Locate every Plasmodium ovale-infected red blood cell.
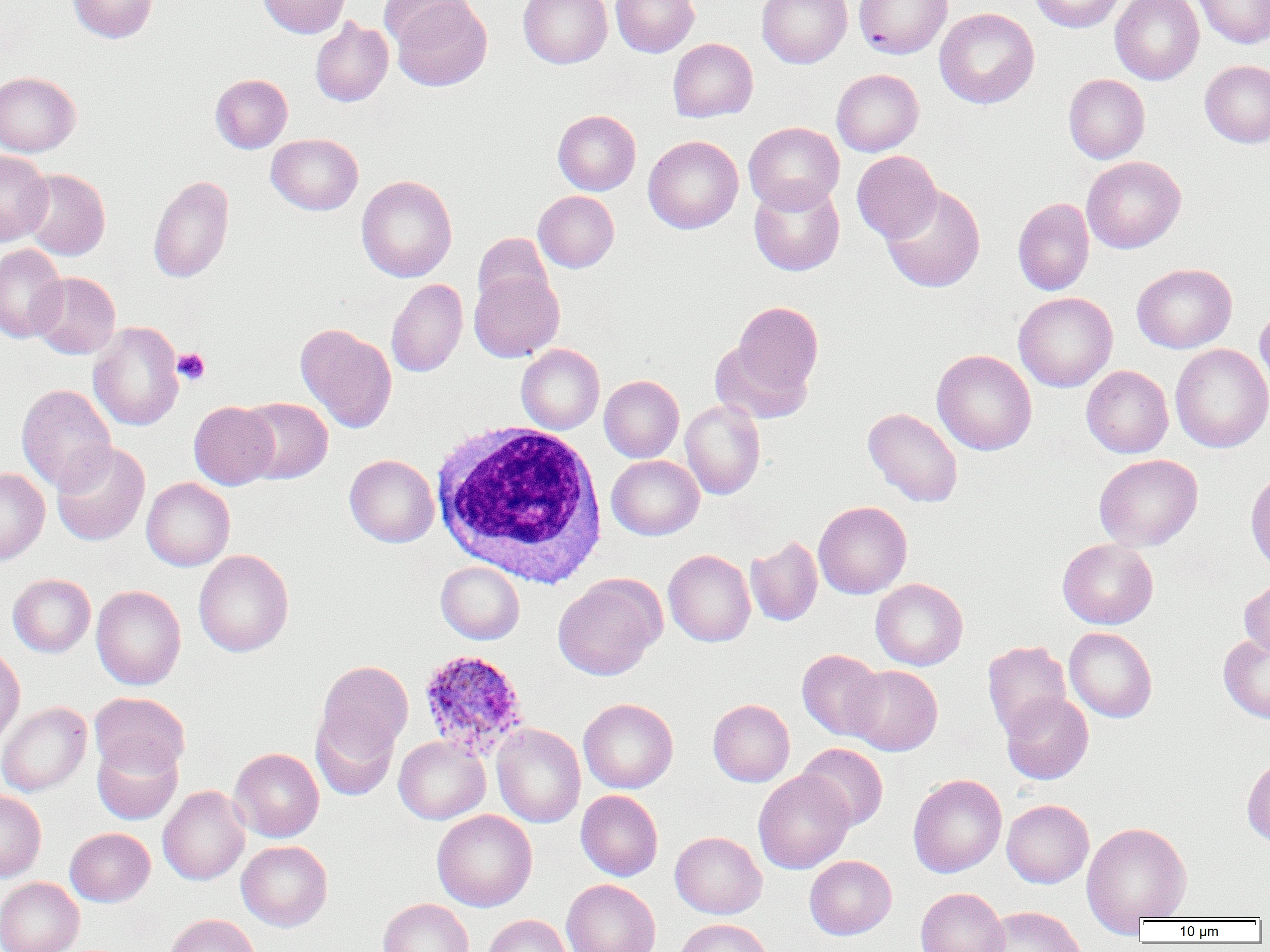

Approximate bounding boxes as named x1/y1/x2/y2 corners in pixels.
Plasmodium ovale-infected red blood cells: (x1=417, y1=648, x2=530, y2=760).

Summary:
  - White blood cell locations: (x1=430, y1=422, x2=609, y2=587)
  - Platelet locations: (x1=173, y1=348, x2=210, y2=385)
  - Uninfected red blood cell locations: (x1=68, y1=0, x2=158, y2=43), (x1=257, y1=0, x2=350, y2=38), (x1=390, y1=0, x2=492, y2=91), (x1=518, y1=0, x2=612, y2=68), (x1=611, y1=0, x2=700, y2=57), (x1=757, y1=0, x2=852, y2=68), (x1=853, y1=0, x2=952, y2=59), (x1=1029, y1=0, x2=1125, y2=33), (x1=1110, y1=0, x2=1204, y2=85), (x1=1192, y1=0, x2=1270, y2=49), (x1=379, y1=2, x2=476, y2=50), (x1=934, y1=8, x2=1039, y2=109), (x1=310, y1=18, x2=393, y2=106), (x1=668, y1=38, x2=758, y2=122), (x1=1200, y1=59, x2=1270, y2=148), (x1=831, y1=69, x2=924, y2=156), (x1=0, y1=71, x2=81, y2=156), (x1=210, y1=74, x2=292, y2=153), (x1=1063, y1=74, x2=1150, y2=164), (x1=553, y1=110, x2=641, y2=195), (x1=744, y1=121, x2=845, y2=214), (x1=266, y1=134, x2=363, y2=215), (x1=643, y1=135, x2=743, y2=234), (x1=0, y1=150, x2=53, y2=245), (x1=852, y1=150, x2=942, y2=243), (x1=1082, y1=156, x2=1185, y2=253), (x1=20, y1=168, x2=110, y2=260), (x1=148, y1=175, x2=234, y2=283), (x1=356, y1=175, x2=457, y2=282), (x1=749, y1=179, x2=845, y2=276), (x1=880, y1=184, x2=986, y2=293), (x1=533, y1=190, x2=619, y2=272), (x1=1013, y1=198, x2=1094, y2=295), (x1=473, y1=233, x2=553, y2=313), (x1=0, y1=244, x2=67, y2=343), (x1=1132, y1=263, x2=1237, y2=353), (x1=469, y1=270, x2=564, y2=362), (x1=28, y1=272, x2=120, y2=359), (x1=386, y1=278, x2=468, y2=377), (x1=1013, y1=292, x2=1118, y2=392), (x1=730, y1=301, x2=823, y2=403), (x1=1255, y1=302, x2=1270, y2=397), (x1=88, y1=321, x2=184, y2=431), (x1=295, y1=322, x2=397, y2=433), (x1=709, y1=338, x2=811, y2=424), (x1=1170, y1=343, x2=1270, y2=453), (x1=516, y1=344, x2=604, y2=434), (x1=931, y1=349, x2=1037, y2=455), (x1=1081, y1=365, x2=1173, y2=458), (x1=599, y1=375, x2=684, y2=462), (x1=16, y1=384, x2=116, y2=494), (x1=237, y1=397, x2=333, y2=484), (x1=680, y1=400, x2=766, y2=500), (x1=189, y1=401, x2=279, y2=489), (x1=862, y1=407, x2=963, y2=507), (x1=51, y1=441, x2=150, y2=546), (x1=1093, y1=453, x2=1203, y2=552), (x1=344, y1=454, x2=439, y2=547), (x1=607, y1=455, x2=704, y2=540), (x1=0, y1=467, x2=50, y2=566), (x1=1245, y1=468, x2=1270, y2=574), (x1=141, y1=477, x2=235, y2=571), (x1=814, y1=501, x2=912, y2=599), (x1=745, y1=535, x2=822, y2=627), (x1=1057, y1=538, x2=1158, y2=629), (x1=193, y1=549, x2=294, y2=657), (x1=663, y1=549, x2=755, y2=647), (x1=435, y1=561, x2=525, y2=644), (x1=8, y1=573, x2=96, y2=657), (x1=553, y1=574, x2=665, y2=680), (x1=1239, y1=577, x2=1270, y2=660), (x1=870, y1=578, x2=968, y2=670), (x1=91, y1=585, x2=186, y2=690), (x1=1064, y1=627, x2=1157, y2=723), (x1=1218, y1=634, x2=1270, y2=724), (x1=982, y1=640, x2=1071, y2=738), (x1=0, y1=646, x2=25, y2=749), (x1=797, y1=649, x2=886, y2=741), (x1=315, y1=660, x2=414, y2=762), (x1=846, y1=665, x2=943, y2=755), (x1=89, y1=692, x2=190, y2=778), (x1=1001, y1=692, x2=1093, y2=784), (x1=579, y1=698, x2=678, y2=793), (x1=708, y1=698, x2=795, y2=786), (x1=0, y1=699, x2=189, y2=787), (x1=0, y1=702, x2=91, y2=796), (x1=310, y1=710, x2=399, y2=801), (x1=491, y1=724, x2=586, y2=828), (x1=394, y1=736, x2=490, y2=824), (x1=92, y1=738, x2=182, y2=824), (x1=796, y1=743, x2=888, y2=831), (x1=229, y1=748, x2=324, y2=842), (x1=1241, y1=754, x2=1270, y2=846), (x1=754, y1=770, x2=854, y2=874), (x1=907, y1=773, x2=1007, y2=878), (x1=158, y1=785, x2=250, y2=885), (x1=0, y1=790, x2=46, y2=882), (x1=576, y1=790, x2=663, y2=881), (x1=1001, y1=799, x2=1094, y2=888), (x1=432, y1=809, x2=537, y2=911), (x1=1082, y1=821, x2=1192, y2=926), (x1=65, y1=827, x2=155, y2=906), (x1=670, y1=832, x2=767, y2=919), (x1=236, y1=840, x2=332, y2=931), (x1=805, y1=855, x2=897, y2=939), (x1=0, y1=877, x2=84, y2=952), (x1=562, y1=879, x2=660, y2=952), (x1=916, y1=887, x2=1009, y2=952), (x1=378, y1=898, x2=473, y2=952), (x1=980, y1=905, x2=1085, y2=952), (x1=164, y1=914, x2=260, y2=952), (x1=482, y1=914, x2=572, y2=952), (x1=674, y1=918, x2=774, y2=952)
  - Slide-level diagnosis: Plasmodium ovale
  - Modality: light microscopy
  - Image size: 1270×952 pixels
  - Field of view: single
  - Magnification: 1000x
  - Preparation: thin blood smear